Point out each Plasmodium parasite.
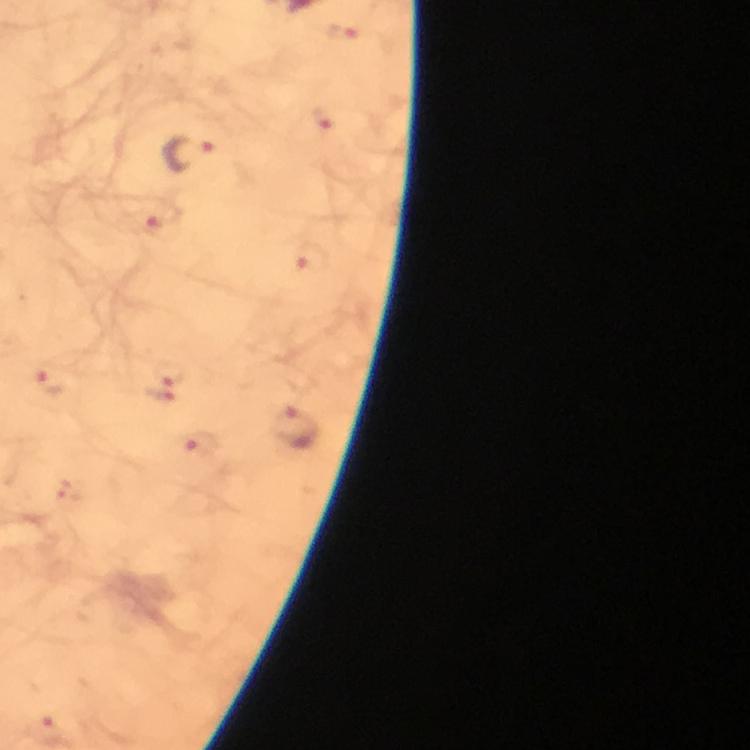

Approximate centers as {x, y} in pixels.
Plasmodium parasites: {340, 33}, {320, 119}, {191, 154}, {149, 221}, {313, 259}, {171, 370}, {50, 383}, {160, 394}, {297, 431}, {199, 444}, {71, 491}, {50, 731}.

Summary:
  - Immersion oil: applied
  - Image size: 750×750 pixels
  - Capture: smartphone camera through the microscope
  - Cropped from: one field of view
  - Magnification: 100x
  - Preparation: thick blood film
  - Stain: Giemsa
  - Context: from a diagnostic examination for malaria